Assess this cell for malaria.
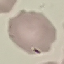
Uninfected.

Acquired by smartphone through the microscope eyepiece. Giemsa-stained preparation. Thin blood smear. Cell patch, automatically extracted from a larger field of view and resized to 64 × 64 pixels.